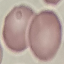
Result: no malaria parasites detected. Acquired by smartphone through the microscope eyepiece. Giemsa stain. Thin smear of blood. Automatically extracted cell patch, resized to 64 × 64 pixels.